Report the malaria status of this cell.
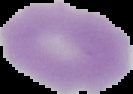

It is uninfected.

Summary:
  - Image size: 133×94 pixels
  - Preparation: thin blood smear
  - Image type: segmented cell region with the area outside set to black